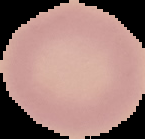
Summary:
  - Preparation: thin blood smear
  - Image type: segmented cell region with the area outside set to black
  - Image size: 145×139 pixels
  - Malaria status: uninfected